Report the malaria status of this cell.
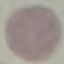

Uninfected.

Giemsa stain. Thin blood smear. Acquired by smartphone through the microscope eyepiece. Automatically extracted cell patch, resized to 64 × 64 pixels.